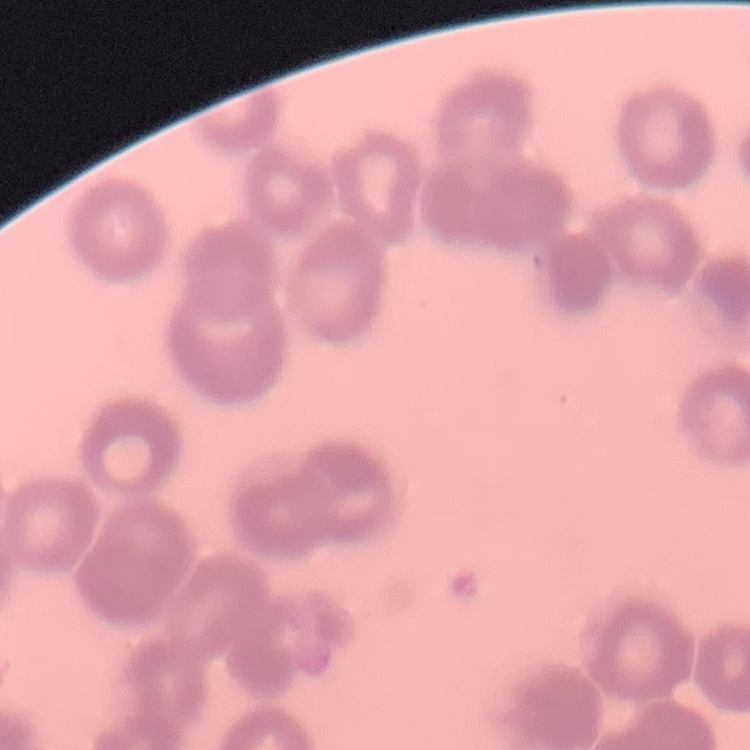
red blood cell morphology = rouleaux formation
stain = Field's or Giemsa
image type = one tile cut from a larger photomicrograph
preparation = thin blood film